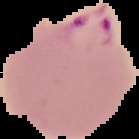

Image is 139×139 pixels. The area outside the segmented cell region is set to black. Malaria status: parasitized. From a thin blood smear.